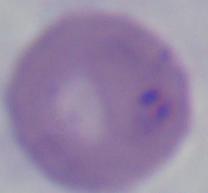
Summary:
  - Magnification: 1000x
  - Identification: Babesia
  - Modality: micrograph